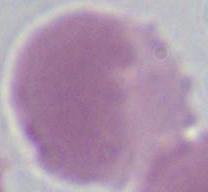
Summary:
  - Modality: micrograph
  - Magnification: 1000x
  - Identification: red blood cell